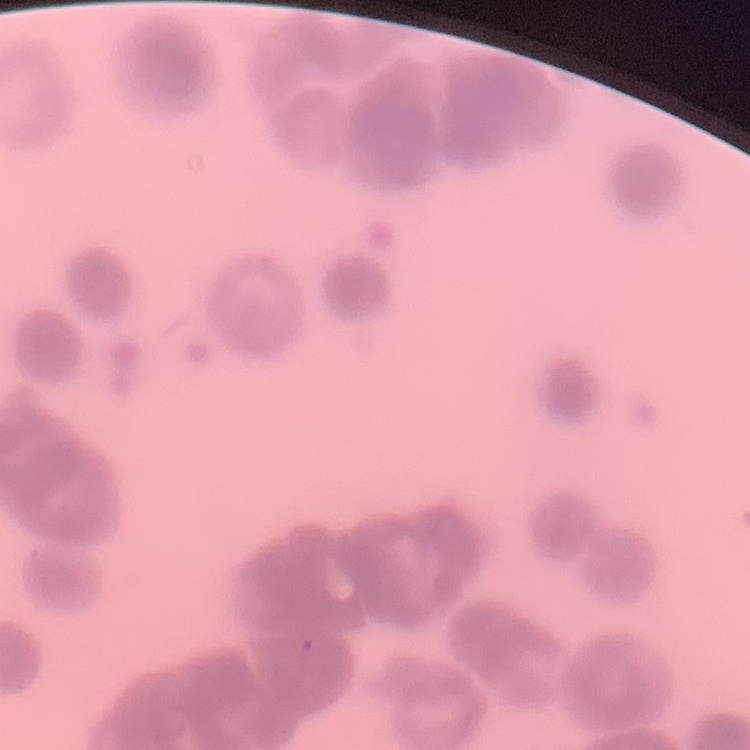
erythrocyte morphology = rouleaux formation
image type = square crop of a larger photomicrograph
stain = Field's or Giemsa
preparation = thin blood film